Point out each leukocyte.
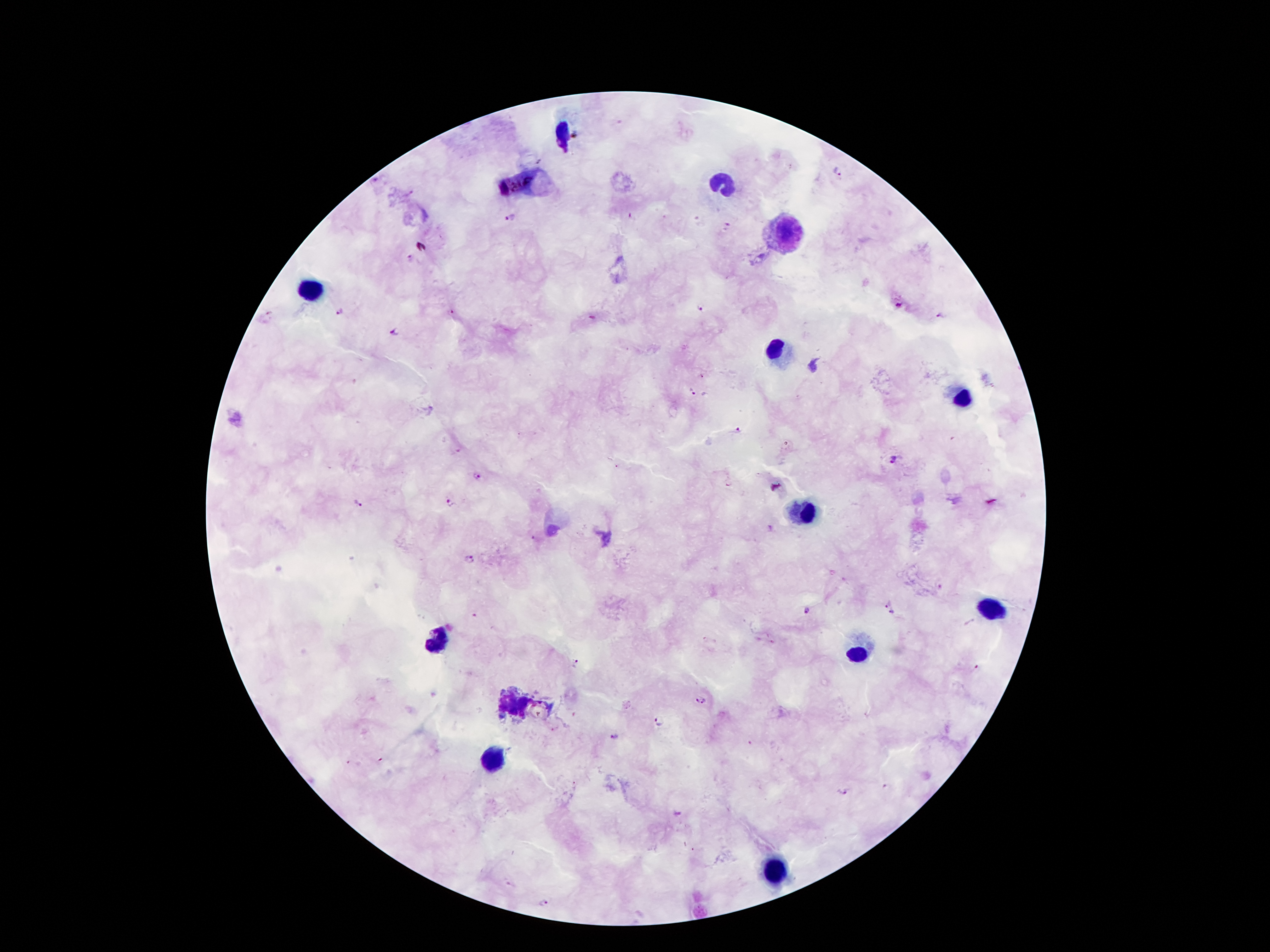
Approximate centers as {x, y} in pixels.
Leukocytes: {562, 133}, {724, 187}, {787, 236}, {310, 292}, {778, 353}, {961, 397}, {806, 514}, {993, 609}, {440, 640}, {860, 655}, {493, 762}, {774, 875}.

Summary:
  - Plasmodium parasite locations: {840, 172}, {509, 218}, {409, 258}, {899, 306}, {341, 310}, {701, 310}, {450, 311}, {944, 316}, {396, 331}, {692, 392}, {736, 430}, {894, 462}, {476, 476}, {359, 503}, {450, 503}, {469, 558}, {888, 602}, {808, 611}, {892, 612}, {474, 616}, {575, 663}, {977, 667}, {701, 699}, {659, 721}, {615, 736}, {886, 788}, {842, 792}, {677, 815}, {511, 884}, {545, 903}
  - Stain: Giemsa
  - Capture: smartphone camera through the microscope eyepiece
  - Field of view: one from this slide
  - Magnification: 100x
  - Preparation: thick blood smear
  - Patient malaria status: infected with Plasmodium falciparum
  - Image size: 1270×952 pixels